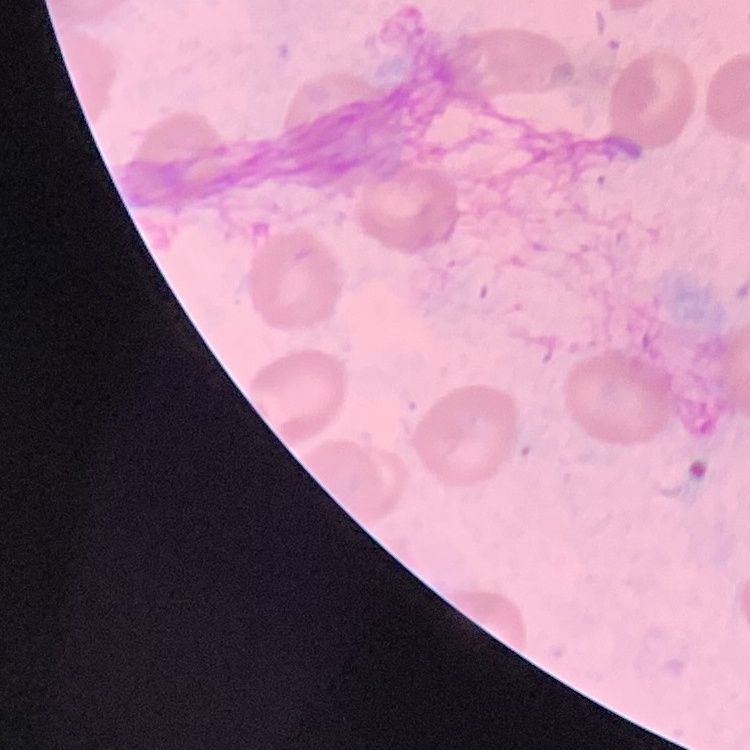
erythrocyte morphology = no rouleaux formation
stain = Field's or Giemsa
image type = one tile cut from a larger photomicrograph
preparation = thin peripheral smear